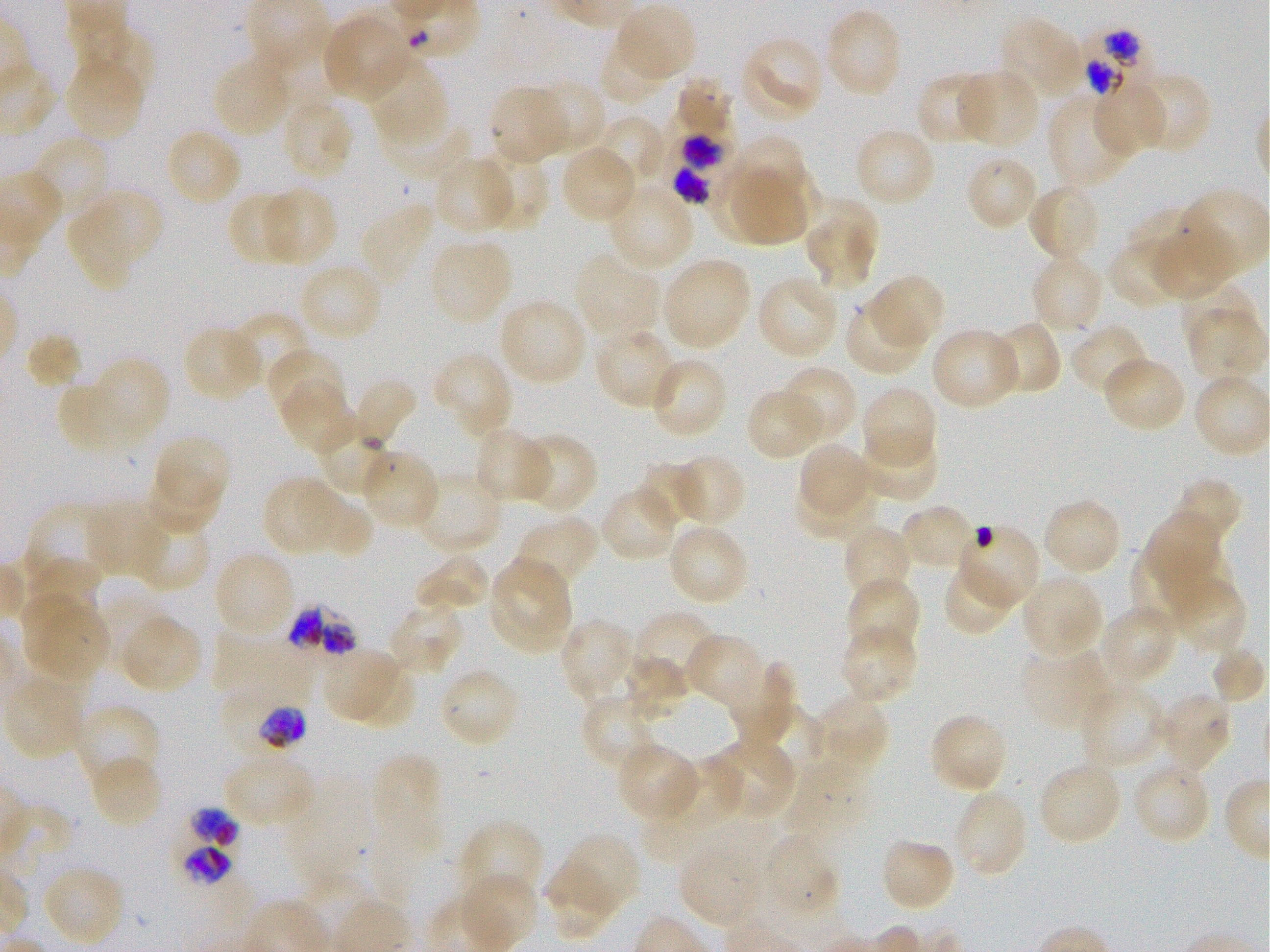

Not every red blood cell is marked. A life-cycle stage — or a range of stages, where the recorded stages span more than one — follows each staged infected red blood cell.
preparation = thin blood film
stain = Giemsa
donor blood group = O+
locations of uninfected red blood cells = approximate bounding boxes as [x1, y1, x2, y2] in pixels: [616, 5, 697, 83], [825, 7, 904, 99], [322, 14, 410, 101], [997, 18, 1083, 99], [79, 23, 155, 99], [598, 36, 671, 106], [742, 37, 824, 119], [365, 54, 448, 144], [212, 55, 293, 138], [65, 58, 144, 143], [958, 69, 1040, 148], [916, 71, 997, 146], [1133, 71, 1213, 156], [675, 76, 733, 137], [1092, 79, 1166, 156], [532, 80, 607, 155], [487, 86, 567, 164], [1048, 95, 1134, 190], [282, 97, 354, 181], [380, 114, 473, 182], [592, 115, 666, 188], [853, 126, 937, 207], [165, 127, 243, 207], [731, 135, 807, 212], [31, 136, 110, 219], [560, 145, 637, 224], [479, 151, 550, 231], [431, 155, 516, 234], [964, 155, 1039, 232], [756, 166, 821, 230], [737, 167, 806, 244], [708, 168, 774, 242], [1027, 182, 1101, 263], [607, 185, 695, 271], [262, 186, 337, 265], [83, 187, 164, 264], [226, 190, 297, 266], [1178, 190, 1270, 271], [359, 202, 435, 285], [1127, 207, 1201, 275], [67, 208, 135, 291], [804, 213, 876, 288], [1152, 224, 1233, 300], [430, 238, 513, 323], [1108, 238, 1185, 309], [575, 252, 659, 343], [1030, 252, 1105, 335], [662, 258, 752, 351], [298, 262, 383, 342], [869, 274, 945, 352], [756, 275, 841, 359], [1183, 288, 1258, 348], [498, 297, 587, 386], [844, 299, 926, 376], [229, 312, 312, 390], [989, 321, 1061, 397], [1070, 323, 1149, 397], [182, 325, 261, 403], [593, 327, 679, 411], [930, 327, 1023, 411], [24, 333, 83, 392], [268, 348, 346, 422], [432, 352, 514, 436], [1102, 355, 1187, 433], [648, 356, 729, 440], [93, 357, 171, 443], [781, 365, 858, 443], [354, 378, 419, 450], [56, 381, 135, 454], [282, 384, 354, 452], [861, 385, 938, 468], [747, 387, 827, 460], [471, 428, 551, 503], [856, 430, 938, 503], [518, 432, 598, 514], [157, 435, 228, 503], [798, 443, 874, 517], [361, 450, 440, 530], [673, 453, 748, 527], [637, 460, 705, 529], [147, 464, 221, 533], [414, 471, 504, 554], [796, 471, 875, 539], [1172, 475, 1243, 547], [262, 477, 343, 556], [295, 480, 372, 557], [600, 486, 678, 563], [1042, 497, 1123, 577], [86, 502, 164, 577], [25, 503, 112, 588], [900, 503, 980, 572], [1143, 512, 1219, 582], [131, 515, 210, 593], [515, 516, 601, 589], [667, 523, 750, 606], [842, 524, 913, 604], [956, 526, 1040, 609], [1131, 546, 1208, 632], [1153, 548, 1236, 619], [213, 549, 296, 640], [28, 554, 103, 623], [416, 554, 490, 614], [489, 558, 574, 650], [943, 561, 1017, 637], [1020, 573, 1103, 658], [846, 575, 921, 657], [1173, 578, 1246, 655], [22, 590, 85, 671], [387, 600, 464, 676], [1099, 604, 1178, 685], [34, 605, 110, 681], [634, 610, 718, 687], [120, 615, 202, 694], [557, 618, 636, 702], [215, 619, 304, 703], [838, 623, 918, 705], [684, 632, 766, 710], [1211, 646, 1266, 704], [1019, 647, 1110, 731], [325, 648, 404, 724], [621, 656, 690, 720], [727, 661, 797, 747], [350, 666, 415, 727], [437, 666, 521, 749], [4, 674, 86, 760], [1079, 685, 1165, 771], [1155, 691, 1232, 773], [813, 692, 890, 772], [581, 694, 658, 774], [74, 705, 163, 787], [757, 708, 824, 766], [928, 712, 1009, 794], [710, 738, 797, 821], [615, 742, 699, 822], [372, 753, 443, 846], [222, 754, 315, 829], [88, 755, 165, 829], [661, 760, 743, 829], [1132, 762, 1212, 845], [1043, 766, 1119, 842], [283, 781, 374, 889], [952, 789, 1029, 878], [459, 821, 544, 904], [562, 833, 641, 914], [878, 837, 957, 912], [679, 841, 766, 927], [545, 862, 617, 940], [42, 864, 125, 947], [462, 873, 539, 946]
locations of red blood cells of indeterminate infection status = approximate bounding boxes as [x1, y1, x2, y2] in pixels: [316, 416, 395, 493], [784, 761, 867, 838], [766, 833, 840, 909]
locations of infected red blood cells = approximate bounding boxes as [x1, y1, x2, y2] in pixels: [1078, 29, 1148, 97]; [666, 103, 737, 203]; [287, 605, 359, 657]; [216, 689, 307, 752] early trophozoite to late schizont; [171, 808, 241, 887]
field of view = one from this slide
objective = 100x, oil immersion, numerical aperture 1.25
culture = in-vitro P. falciparum strain 3D7, static
image size = 1270×952 pixels